Locate every Plasmodium falciparum-infected red blood cell.
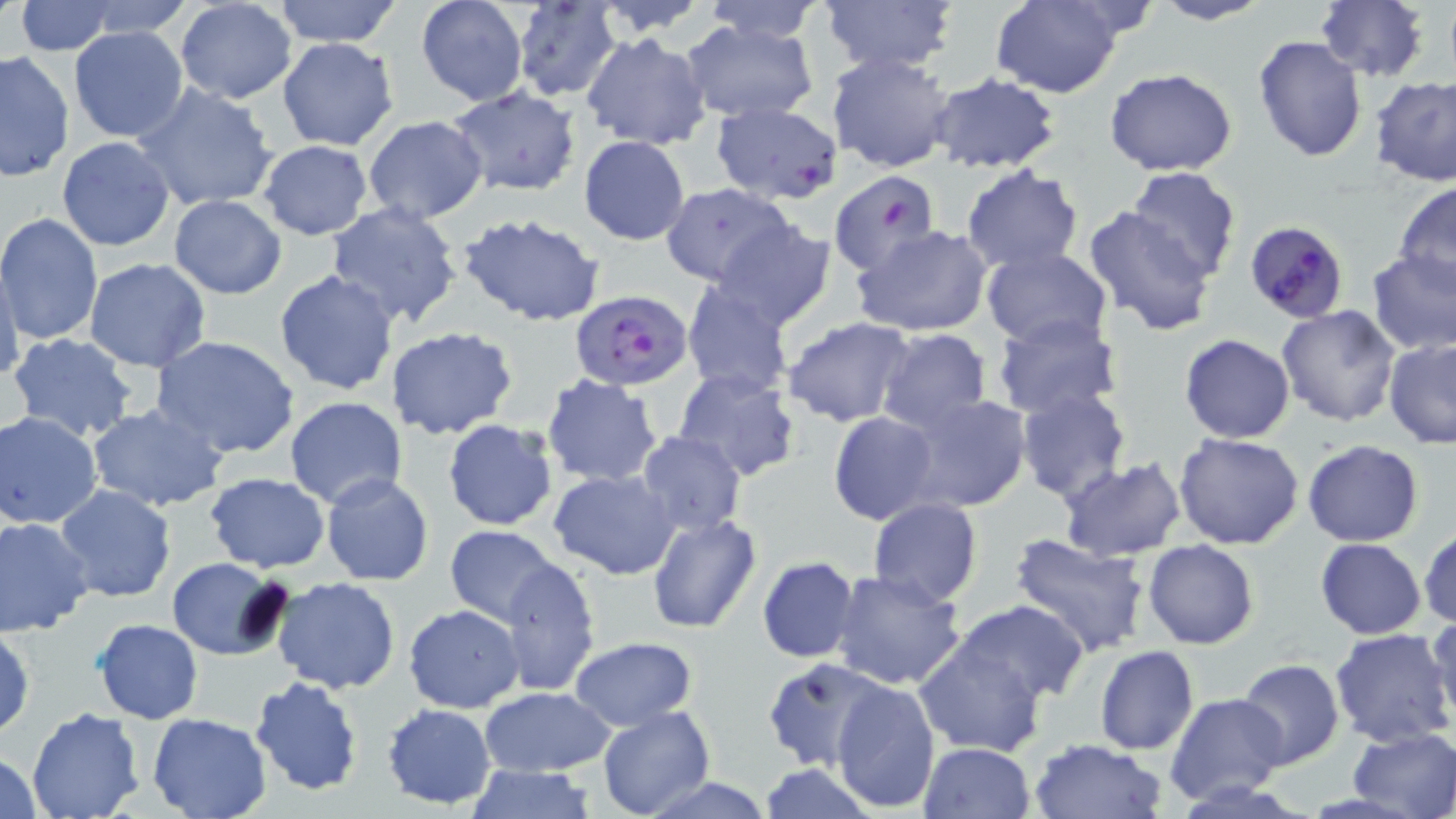

Approximate bounding boxes as named x1/y1/x2/y2 corners in pixels.
Plasmodium falciparum-infected red blood cells: (x1=1245, y1=220, x2=1349, y2=324), (x1=572, y1=290, x2=690, y2=390).

Summary:
  - Uninfected red blood cell locations: (x1=74, y1=0, x2=195, y2=38), (x1=272, y1=0, x2=403, y2=46), (x1=414, y1=0, x2=528, y2=106), (x1=593, y1=0, x2=713, y2=37), (x1=697, y1=0, x2=829, y2=42), (x1=990, y1=0, x2=1127, y2=100), (x1=1151, y1=0, x2=1272, y2=26), (x1=1315, y1=0, x2=1429, y2=82), (x1=14, y1=1, x2=118, y2=55), (x1=822, y1=1, x2=957, y2=77), (x1=175, y1=2, x2=298, y2=103), (x1=512, y1=2, x2=621, y2=101), (x1=679, y1=18, x2=820, y2=123), (x1=68, y1=25, x2=188, y2=142), (x1=581, y1=32, x2=712, y2=151), (x1=1252, y1=35, x2=1368, y2=163), (x1=278, y1=38, x2=399, y2=149), (x1=1, y1=51, x2=74, y2=180), (x1=827, y1=51, x2=958, y2=173), (x1=1105, y1=68, x2=1238, y2=178), (x1=927, y1=70, x2=1062, y2=174), (x1=1370, y1=74, x2=1456, y2=186), (x1=134, y1=83, x2=279, y2=213), (x1=447, y1=88, x2=582, y2=197), (x1=711, y1=100, x2=844, y2=203), (x1=363, y1=116, x2=488, y2=223), (x1=578, y1=135, x2=690, y2=245), (x1=56, y1=136, x2=176, y2=251), (x1=257, y1=140, x2=373, y2=239), (x1=960, y1=165, x2=1084, y2=275), (x1=1127, y1=167, x2=1242, y2=282), (x1=831, y1=169, x2=943, y2=276), (x1=1394, y1=182, x2=1456, y2=292), (x1=660, y1=183, x2=796, y2=287), (x1=169, y1=195, x2=287, y2=298), (x1=325, y1=201, x2=464, y2=327), (x1=1080, y1=204, x2=1220, y2=337), (x1=0, y1=213, x2=103, y2=345), (x1=457, y1=213, x2=605, y2=327), (x1=712, y1=220, x2=837, y2=332), (x1=853, y1=225, x2=994, y2=338), (x1=981, y1=247, x2=1112, y2=348), (x1=1367, y1=250, x2=1456, y2=356), (x1=84, y1=257, x2=210, y2=373), (x1=0, y1=260, x2=25, y2=389), (x1=274, y1=270, x2=400, y2=394), (x1=681, y1=279, x2=796, y2=398), (x1=1276, y1=305, x2=1403, y2=427), (x1=992, y1=309, x2=1124, y2=421), (x1=781, y1=315, x2=917, y2=427), (x1=385, y1=327, x2=519, y2=441), (x1=875, y1=327, x2=991, y2=433), (x1=7, y1=333, x2=138, y2=443), (x1=1179, y1=334, x2=1295, y2=442), (x1=151, y1=335, x2=300, y2=459), (x1=1384, y1=339, x2=1456, y2=449), (x1=673, y1=368, x2=802, y2=485), (x1=541, y1=374, x2=664, y2=486), (x1=1016, y1=388, x2=1132, y2=503), (x1=901, y1=393, x2=1034, y2=514), (x1=284, y1=397, x2=410, y2=510), (x1=86, y1=404, x2=228, y2=513), (x1=1, y1=411, x2=104, y2=529), (x1=828, y1=412, x2=941, y2=525), (x1=443, y1=418, x2=560, y2=532), (x1=638, y1=432, x2=745, y2=536), (x1=1174, y1=432, x2=1306, y2=549), (x1=1302, y1=440, x2=1424, y2=547), (x1=1057, y1=458, x2=1186, y2=564), (x1=550, y1=469, x2=681, y2=579), (x1=205, y1=473, x2=330, y2=572), (x1=320, y1=473, x2=434, y2=587), (x1=53, y1=486, x2=177, y2=603), (x1=867, y1=499, x2=983, y2=607), (x1=645, y1=513, x2=763, y2=635), (x1=0, y1=517, x2=96, y2=638), (x1=1419, y1=524, x2=1455, y2=630), (x1=444, y1=526, x2=560, y2=626), (x1=1009, y1=532, x2=1150, y2=655), (x1=1314, y1=537, x2=1428, y2=638), (x1=1142, y1=538, x2=1258, y2=649), (x1=757, y1=555, x2=859, y2=661), (x1=498, y1=556, x2=600, y2=695), (x1=166, y1=557, x2=289, y2=659), (x1=830, y1=569, x2=966, y2=689), (x1=272, y1=576, x2=401, y2=694), (x1=953, y1=601, x2=1090, y2=704), (x1=404, y1=604, x2=524, y2=713), (x1=1426, y1=612, x2=1456, y2=729), (x1=92, y1=617, x2=203, y2=724), (x1=0, y1=625, x2=35, y2=740), (x1=1329, y1=629, x2=1455, y2=747), (x1=912, y1=635, x2=1047, y2=756), (x1=570, y1=636, x2=697, y2=730), (x1=1093, y1=645, x2=1200, y2=755), (x1=763, y1=657, x2=887, y2=770), (x1=1236, y1=658, x2=1345, y2=769), (x1=248, y1=676, x2=365, y2=796), (x1=830, y1=678, x2=939, y2=812), (x1=480, y1=686, x2=614, y2=777), (x1=1167, y1=692, x2=1288, y2=804), (x1=382, y1=702, x2=496, y2=810), (x1=596, y1=706, x2=715, y2=819), (x1=26, y1=708, x2=145, y2=819), (x1=146, y1=713, x2=272, y2=819), (x1=1346, y1=727, x2=1456, y2=816), (x1=1028, y1=738, x2=1169, y2=819), (x1=920, y1=742, x2=1035, y2=818), (x1=2, y1=749, x2=43, y2=819), (x1=756, y1=763, x2=879, y2=819), (x1=463, y1=764, x2=597, y2=819), (x1=637, y1=775, x2=779, y2=818)
  - Slide-level diagnosis: Plasmodium falciparum
  - Stain: May-Grünwald-Giemsa
  - Preparation: thin blood film
  - Modality: optical microscopy
  - Image size: 1456×819 pixels
  - Field of view: one of a larger specimen
  - Magnification: 1000x